Point out each leukocyte.
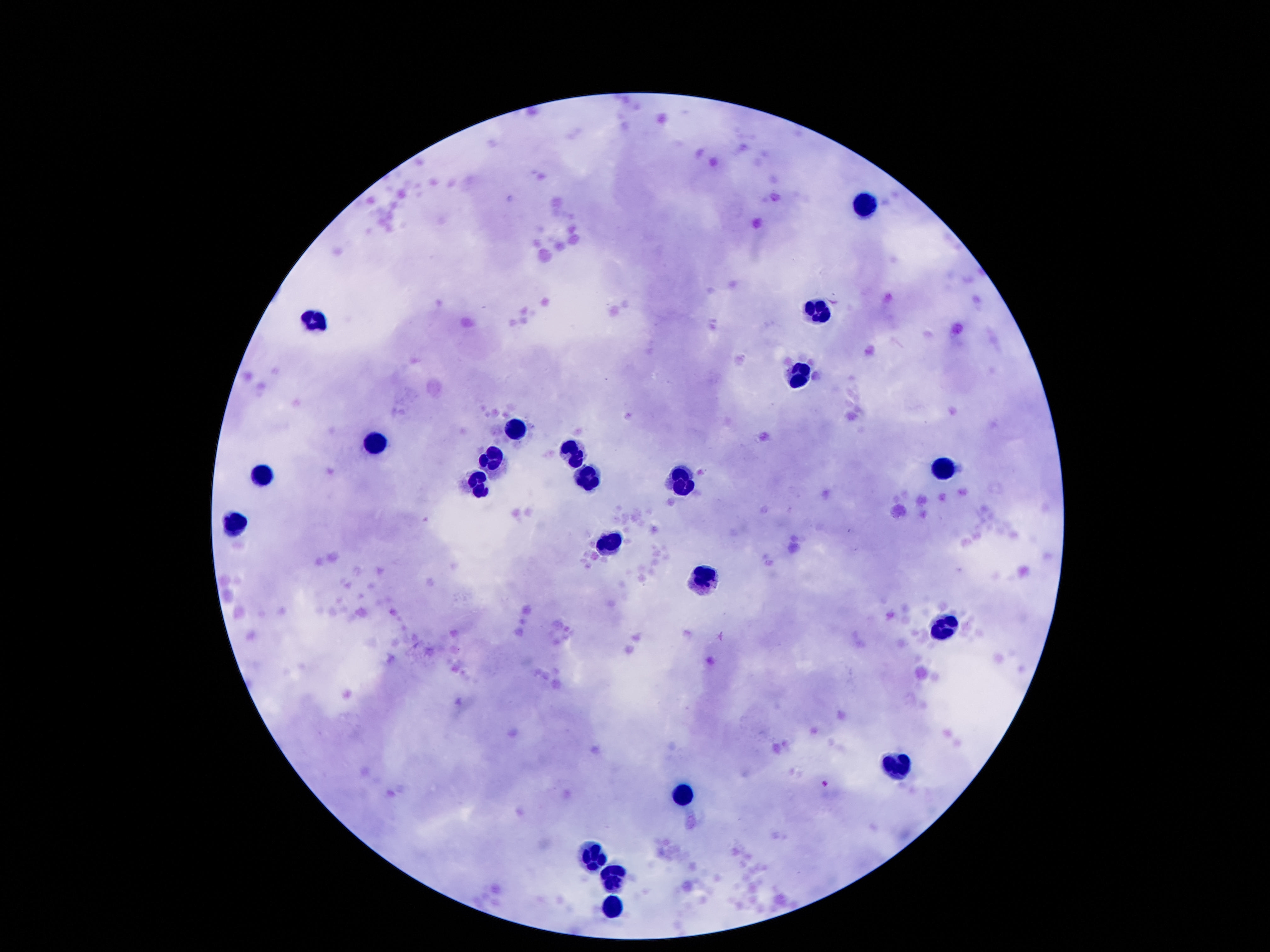

Approximate centers as [x, y] in pixels.
Leukocytes: [867, 203], [820, 310], [315, 312], [800, 371], [508, 433], [375, 448], [573, 450], [493, 458], [259, 465], [943, 468], [585, 475], [681, 478], [471, 480], [236, 522], [610, 539], [706, 576], [941, 628], [896, 767], [686, 796], [590, 853], [615, 875], [615, 905].

Summary:
  - Field of view: one from this slide
  - Patient malaria status: not infected
  - Capture: smartphone camera through the microscope eyepiece
  - Stain: Giemsa
  - Image size: 1270×952 pixels
  - Preparation: thick blood smear
  - Magnification: 100x